Classify this cell by malaria status.
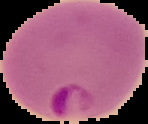
Parasitized.

Summary:
  - Preparation: thin blood film
  - Image size: 148×124 pixels
  - Image type: segmented cell region on a black background